State which cell type is depicted.
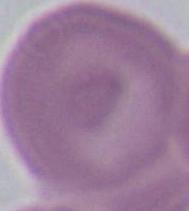
An erythrocyte.

Photomicrograph. 1000x magnification.